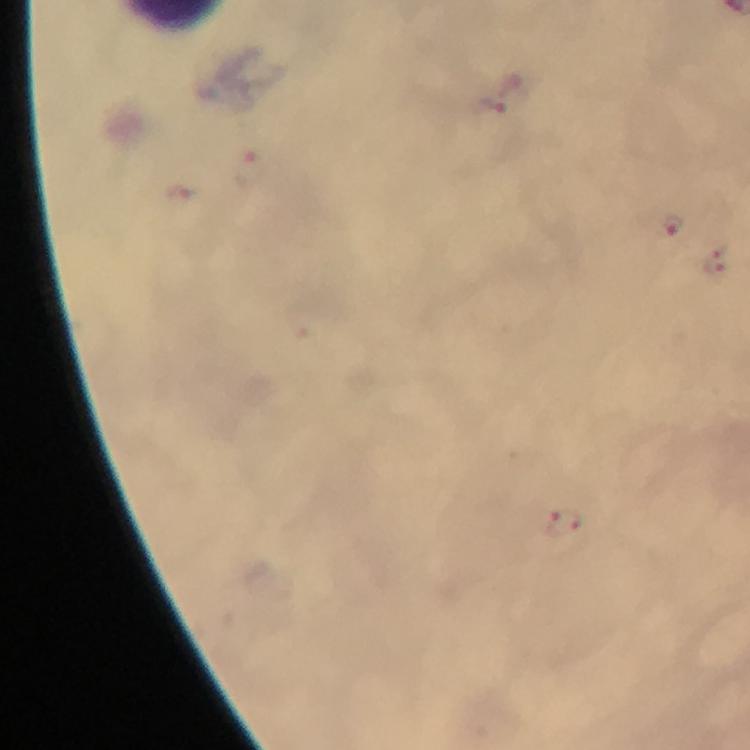 Approximate centers as (x, y) in pixels. Malaria parasite locations: (492, 109), (250, 172), (180, 199), (672, 226), (717, 261), (563, 524). Thick blood film. Giemsa-stained preparation. At 100x magnification. Photographed through the microscope with a smartphone camera. A crop from one field of view. Image is 750×750 pixels. From a diagnostic examination for malaria. Immersion oil applied.